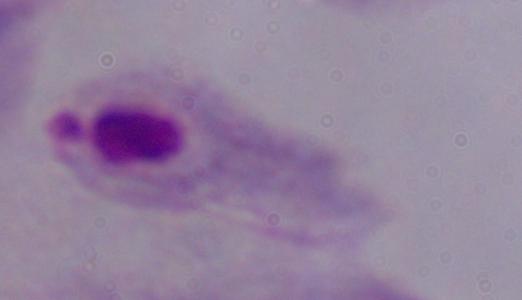
modality = micrograph
magnification = 1000x
identification = trichomonad